Outline each blood parasite and name the species.
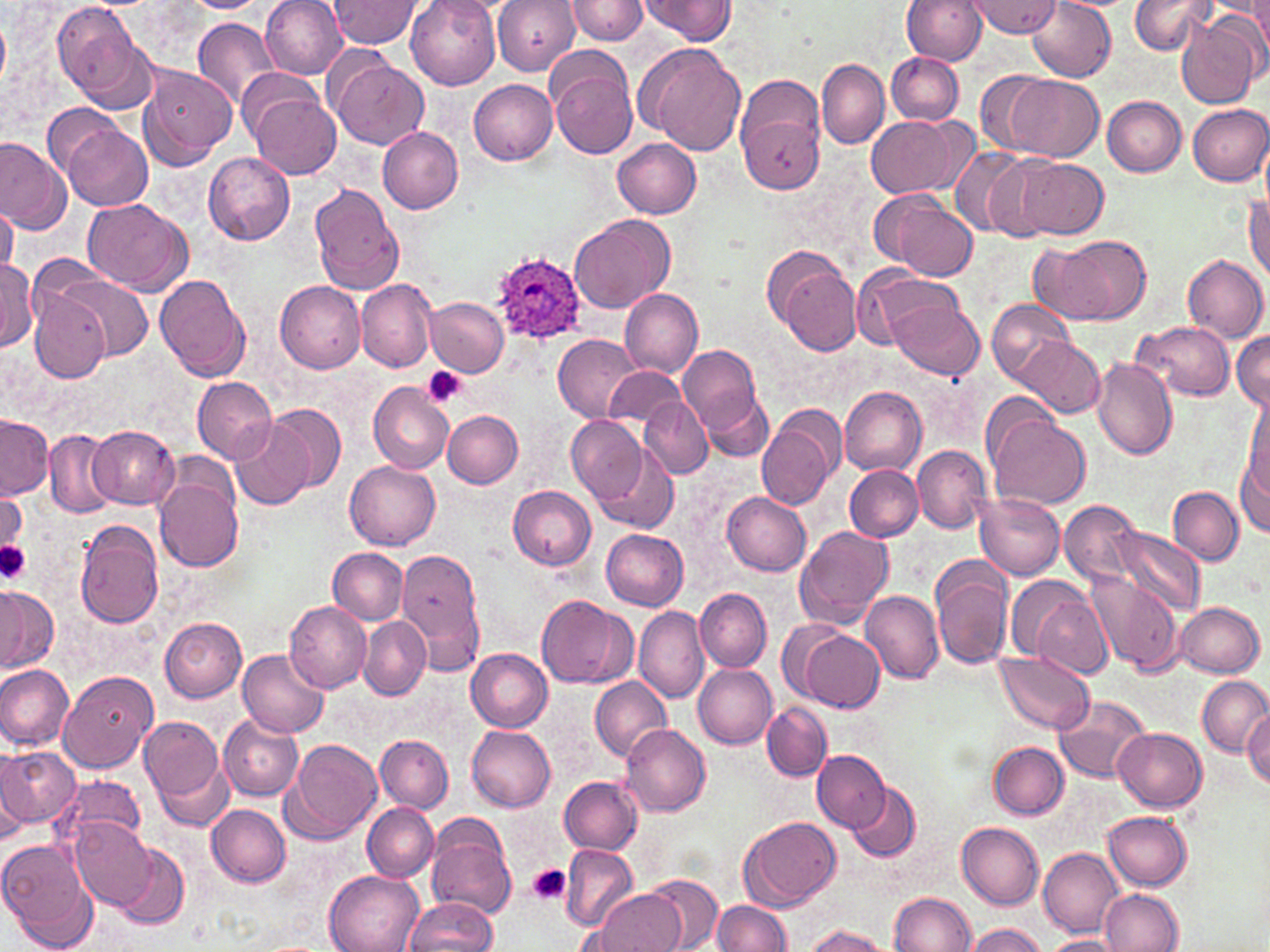
Approximate bounding boxes as named x1/y1/x2/y2 corners in pixels.
Plasmodium ovale-infected red blood cells: (x1=491, y1=248, x2=593, y2=353).
No Plasmodium falciparum, Plasmodium malariae, Plasmodium vivax, Babesia divergens, or Trypanosoma brucei observed.

slide-level diagnosis = Plasmodium ovale
modality = light microscopy
uninfected red blood cell locations = approximate bounding boxes as named x1/y1/x2/y2 corners in pixels: (x1=184, y1=0, x2=267, y2=13), (x1=262, y1=0, x2=348, y2=79), (x1=328, y1=0, x2=421, y2=49), (x1=406, y1=0, x2=499, y2=91), (x1=493, y1=0, x2=582, y2=76), (x1=563, y1=0, x2=649, y2=46), (x1=638, y1=0, x2=738, y2=44), (x1=901, y1=0, x2=987, y2=64), (x1=1249, y1=0, x2=1270, y2=55), (x1=1128, y1=1, x2=1215, y2=56), (x1=970, y1=2, x2=1061, y2=37), (x1=1029, y1=2, x2=1116, y2=81), (x1=53, y1=3, x2=154, y2=110), (x1=1218, y1=5, x2=1270, y2=78), (x1=1178, y1=13, x2=1264, y2=110), (x1=0, y1=17, x2=9, y2=91), (x1=192, y1=18, x2=281, y2=106), (x1=640, y1=44, x2=748, y2=156), (x1=548, y1=52, x2=639, y2=160), (x1=887, y1=53, x2=964, y2=125), (x1=328, y1=57, x2=429, y2=150), (x1=817, y1=58, x2=888, y2=150), (x1=137, y1=62, x2=237, y2=170), (x1=237, y1=68, x2=327, y2=142), (x1=976, y1=68, x2=1060, y2=158), (x1=1004, y1=74, x2=1104, y2=162), (x1=468, y1=79, x2=558, y2=165), (x1=248, y1=90, x2=342, y2=180), (x1=736, y1=90, x2=825, y2=196), (x1=1102, y1=96, x2=1187, y2=177), (x1=43, y1=102, x2=130, y2=178), (x1=1187, y1=104, x2=1270, y2=186), (x1=866, y1=114, x2=962, y2=197), (x1=61, y1=125, x2=153, y2=211), (x1=377, y1=126, x2=464, y2=214), (x1=0, y1=136, x2=70, y2=235), (x1=613, y1=138, x2=702, y2=219), (x1=951, y1=149, x2=1051, y2=241), (x1=204, y1=152, x2=295, y2=245), (x1=1017, y1=157, x2=1108, y2=239), (x1=310, y1=183, x2=406, y2=297), (x1=874, y1=191, x2=979, y2=282), (x1=1245, y1=192, x2=1270, y2=280), (x1=83, y1=199, x2=190, y2=293), (x1=1, y1=203, x2=17, y2=278), (x1=570, y1=214, x2=676, y2=314), (x1=1035, y1=233, x2=1151, y2=326), (x1=766, y1=246, x2=862, y2=353), (x1=1182, y1=254, x2=1269, y2=343), (x1=0, y1=260, x2=39, y2=351), (x1=852, y1=264, x2=961, y2=351), (x1=154, y1=274, x2=250, y2=381), (x1=55, y1=276, x2=153, y2=362), (x1=354, y1=279, x2=438, y2=372), (x1=275, y1=281, x2=367, y2=373), (x1=619, y1=289, x2=703, y2=377), (x1=29, y1=291, x2=112, y2=383), (x1=425, y1=297, x2=509, y2=377), (x1=889, y1=299, x2=984, y2=378), (x1=987, y1=299, x2=1078, y2=386), (x1=569, y1=309, x2=701, y2=407), (x1=1132, y1=321, x2=1234, y2=400), (x1=1233, y1=331, x2=1270, y2=412), (x1=554, y1=335, x2=641, y2=422), (x1=1014, y1=338, x2=1106, y2=418), (x1=679, y1=344, x2=767, y2=439), (x1=1091, y1=356, x2=1177, y2=460), (x1=605, y1=367, x2=687, y2=429), (x1=192, y1=375, x2=277, y2=466), (x1=369, y1=382, x2=454, y2=474), (x1=840, y1=386, x2=926, y2=476), (x1=703, y1=392, x2=777, y2=460), (x1=1245, y1=394, x2=1270, y2=491), (x1=640, y1=397, x2=713, y2=479), (x1=268, y1=404, x2=347, y2=491), (x1=441, y1=410, x2=523, y2=487), (x1=757, y1=410, x2=841, y2=511), (x1=988, y1=412, x2=1090, y2=510), (x1=0, y1=414, x2=53, y2=499), (x1=566, y1=416, x2=648, y2=504), (x1=229, y1=417, x2=316, y2=511), (x1=89, y1=425, x2=178, y2=510), (x1=45, y1=431, x2=118, y2=518), (x1=592, y1=442, x2=678, y2=535), (x1=913, y1=444, x2=991, y2=533), (x1=1235, y1=448, x2=1269, y2=538), (x1=345, y1=459, x2=441, y2=549), (x1=844, y1=465, x2=924, y2=541), (x1=153, y1=473, x2=245, y2=572), (x1=507, y1=484, x2=597, y2=571), (x1=0, y1=487, x2=25, y2=550), (x1=1168, y1=487, x2=1244, y2=567), (x1=722, y1=492, x2=812, y2=577), (x1=974, y1=492, x2=1066, y2=578), (x1=1060, y1=501, x2=1143, y2=585), (x1=74, y1=519, x2=165, y2=630), (x1=794, y1=525, x2=895, y2=630), (x1=1111, y1=526, x2=1205, y2=617), (x1=601, y1=527, x2=689, y2=610), (x1=396, y1=546, x2=487, y2=673), (x1=329, y1=548, x2=409, y2=625), (x1=931, y1=560, x2=1013, y2=670), (x1=1086, y1=571, x2=1183, y2=676), (x1=1021, y1=579, x2=1113, y2=679), (x1=0, y1=585, x2=54, y2=673), (x1=695, y1=589, x2=772, y2=672), (x1=860, y1=591, x2=943, y2=685), (x1=538, y1=595, x2=633, y2=689), (x1=284, y1=600, x2=371, y2=694), (x1=1175, y1=601, x2=1264, y2=677), (x1=634, y1=607, x2=709, y2=705), (x1=158, y1=616, x2=248, y2=703), (x1=358, y1=616, x2=430, y2=700), (x1=801, y1=630, x2=884, y2=712), (x1=467, y1=648, x2=553, y2=732), (x1=238, y1=649, x2=326, y2=738), (x1=994, y1=652, x2=1095, y2=734), (x1=0, y1=662, x2=73, y2=750), (x1=693, y1=664, x2=778, y2=749), (x1=58, y1=670, x2=156, y2=773), (x1=1198, y1=675, x2=1270, y2=758), (x1=589, y1=676, x2=671, y2=762), (x1=1054, y1=694, x2=1151, y2=784), (x1=762, y1=701, x2=832, y2=782), (x1=1243, y1=710, x2=1270, y2=788), (x1=137, y1=713, x2=227, y2=813), (x1=218, y1=714, x2=304, y2=800), (x1=620, y1=723, x2=711, y2=815), (x1=467, y1=726, x2=557, y2=812), (x1=1115, y1=727, x2=1208, y2=811), (x1=375, y1=733, x2=453, y2=812), (x1=284, y1=739, x2=383, y2=844), (x1=989, y1=741, x2=1068, y2=819), (x1=0, y1=746, x2=78, y2=829), (x1=812, y1=748, x2=890, y2=832), (x1=0, y1=752, x2=29, y2=847), (x1=54, y1=774, x2=148, y2=856), (x1=558, y1=776, x2=643, y2=854), (x1=846, y1=782, x2=921, y2=861), (x1=207, y1=804, x2=292, y2=889), (x1=362, y1=804, x2=438, y2=882), (x1=1104, y1=811, x2=1194, y2=890), (x1=425, y1=816, x2=516, y2=918), (x1=740, y1=816, x2=842, y2=912), (x1=70, y1=817, x2=155, y2=911), (x1=956, y1=822, x2=1044, y2=910), (x1=0, y1=840, x2=99, y2=952), (x1=112, y1=841, x2=190, y2=929), (x1=560, y1=844, x2=638, y2=932), (x1=1040, y1=847, x2=1124, y2=936), (x1=325, y1=870, x2=424, y2=952), (x1=644, y1=873, x2=723, y2=951), (x1=1102, y1=888, x2=1182, y2=952), (x1=594, y1=889, x2=686, y2=952), (x1=888, y1=891, x2=974, y2=951), (x1=404, y1=897, x2=497, y2=951), (x1=712, y1=898, x2=791, y2=951), (x1=964, y1=923, x2=1046, y2=952), (x1=803, y1=925, x2=892, y2=952), (x1=1043, y1=934, x2=1123, y2=952)
image size = 1270×952 pixels
field of view = single
stain = May-Grünwald-Giemsa
magnification = 1000x
preparation = thin blood smear
platelet locations = approximate bounding boxes as named x1/y1/x2/y2 corners in pixels: (x1=421, y1=366, x2=467, y2=408), (x1=0, y1=540, x2=31, y2=584), (x1=528, y1=863, x2=571, y2=905)